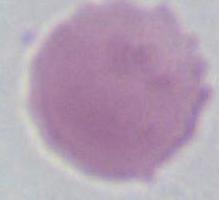
Summary:
  - Modality: photomicrograph
  - Magnification: 1000x
  - Identification: erythrocyte